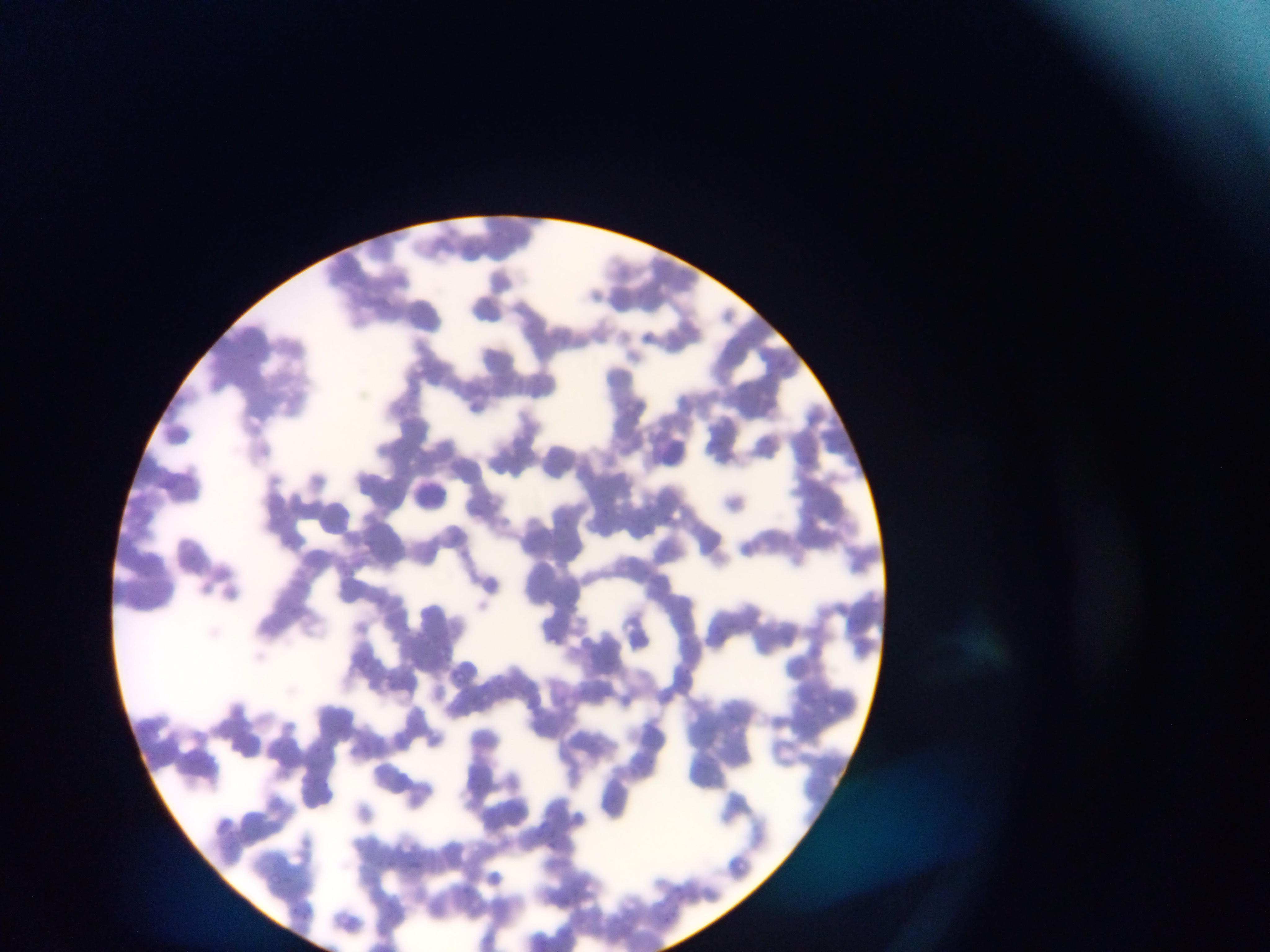
Approximate bounding boxes as (left, top, right, bottom) in pixels.
Summary:
  - Leukocyte locations: (661, 439, 686, 465), (417, 477, 452, 512), (320, 499, 350, 534)
  - Image size: 1270×952 pixels
  - Capture: mobile-phone photograph through a microscope
  - Country: Ghana
  - Field of view: single
  - Preparation: thin blood smear